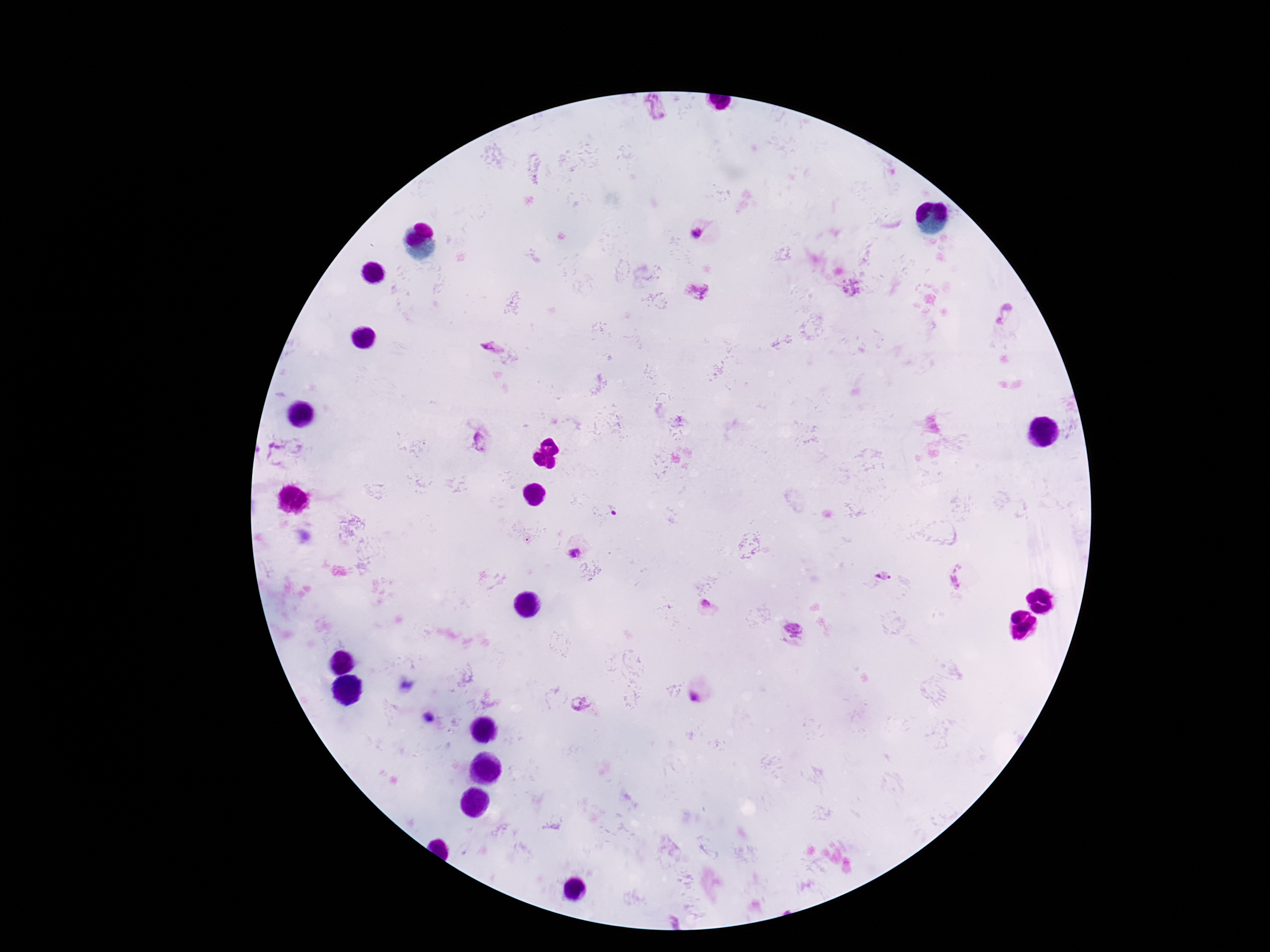
Approximate centers as {x, y} in pixels.
Summary:
  - Plasmodium parasite locations: {655, 109}, {698, 235}, {698, 287}, {851, 288}, {1004, 314}, {492, 349}, {478, 442}, {574, 552}, {884, 576}, {960, 577}, {706, 605}, {793, 628}, {694, 698}, {581, 704}
  - Capture: smartphone camera through the microscope eyepiece
  - Preparation: thick blood smear
  - Patient malaria status: positive
  - Field of view: one from this slide
  - Image size: 1270×952 pixels
  - Stain: Giemsa
  - Magnification: 100x